Outline each uninfected red blood cell.
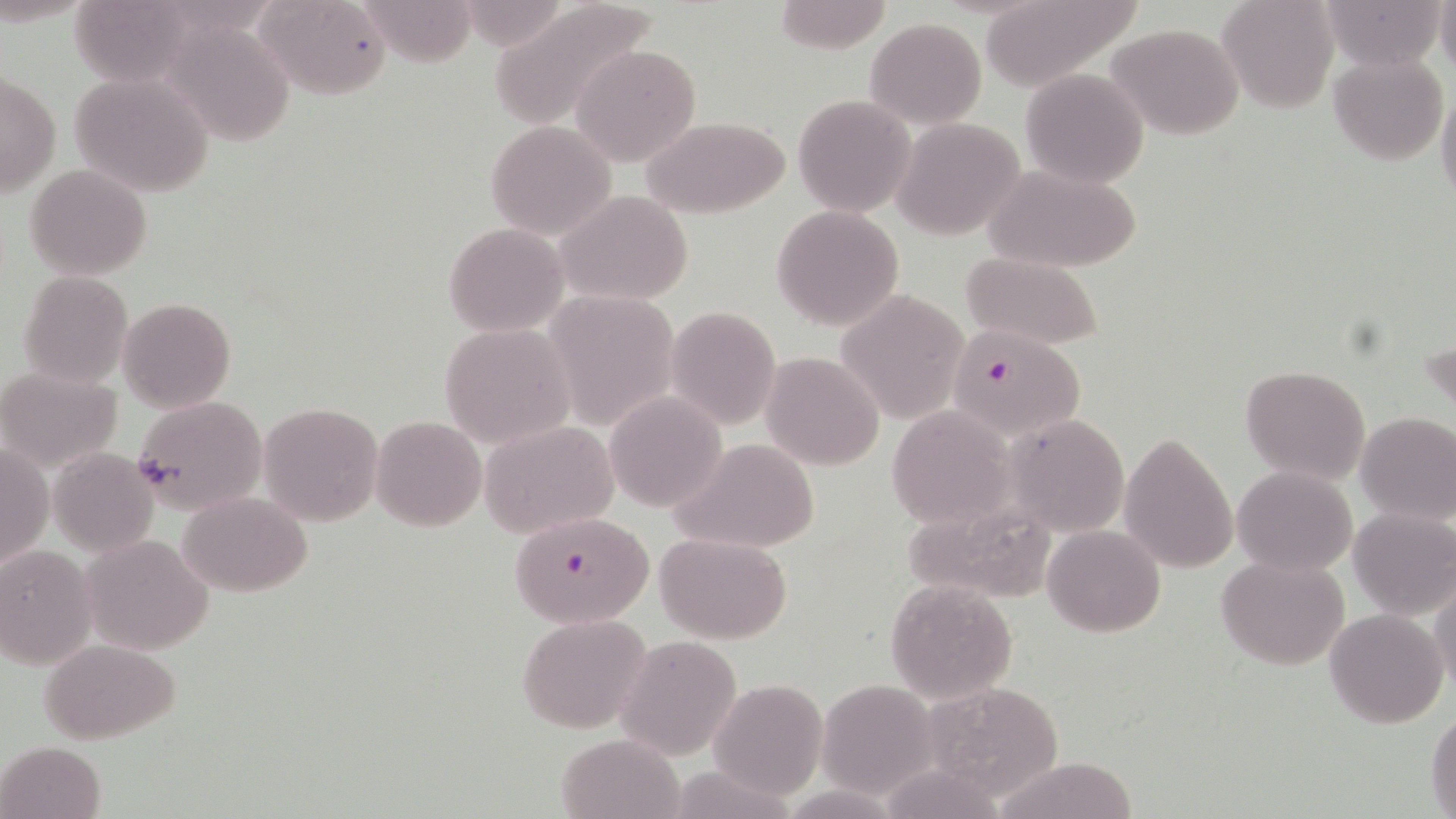
Approximate bounding boxes as [x1, y1, x2, y2] in pixels.
Uninfected red blood cells: [259, 0, 392, 99], [355, 0, 477, 66], [980, 0, 1137, 90], [1218, 0, 1339, 114], [1319, 0, 1447, 70], [770, 1, 890, 52], [487, 3, 659, 127], [864, 18, 986, 128], [164, 20, 300, 147], [1104, 23, 1247, 140], [572, 44, 700, 166], [1328, 52, 1449, 165], [1020, 69, 1148, 187], [69, 70, 215, 197], [1, 73, 61, 197], [1436, 82, 1456, 209], [793, 95, 915, 216], [642, 116, 792, 219], [893, 117, 1026, 242], [485, 119, 618, 241], [25, 164, 152, 279], [985, 164, 1141, 274], [556, 191, 695, 305], [772, 205, 904, 331], [443, 223, 567, 336], [962, 252, 1103, 348], [16, 271, 134, 388], [834, 290, 968, 425], [542, 291, 679, 430], [118, 297, 235, 413], [665, 307, 780, 429], [440, 324, 573, 447], [761, 352, 884, 470], [1239, 364, 1371, 485], [0, 365, 122, 471], [605, 393, 725, 511], [133, 395, 267, 517], [257, 401, 384, 527], [886, 405, 1016, 529], [1355, 411, 1456, 526], [1005, 414, 1128, 535], [371, 415, 486, 531], [479, 420, 620, 538], [1119, 432, 1238, 575], [670, 438, 824, 554], [1, 442, 50, 574], [47, 449, 158, 556], [1233, 466, 1357, 575], [179, 491, 312, 596], [892, 499, 1058, 603], [1348, 506, 1456, 620], [1043, 524, 1165, 636], [655, 533, 791, 642], [82, 534, 213, 653], [0, 546, 98, 667], [1216, 555, 1350, 672], [1430, 573, 1456, 694], [885, 579, 1019, 703], [1324, 609, 1450, 728], [517, 613, 653, 734], [617, 636, 742, 759], [38, 638, 183, 745], [710, 678, 829, 800], [816, 679, 939, 798], [919, 679, 1066, 800], [1427, 708, 1456, 815], [557, 732, 684, 819], [0, 741, 106, 819], [990, 756, 1144, 819].

Plasmodium falciparum-infected red blood cell locations: [943, 325, 1085, 440], [507, 509, 656, 628]. Slide-level diagnosis: Plasmodium falciparum. Single field of view. Captured at 1000x magnification. May-Grünwald-Giemsa stain. Image is 1456×819 pixels. Thin blood smear. Light microscopy.